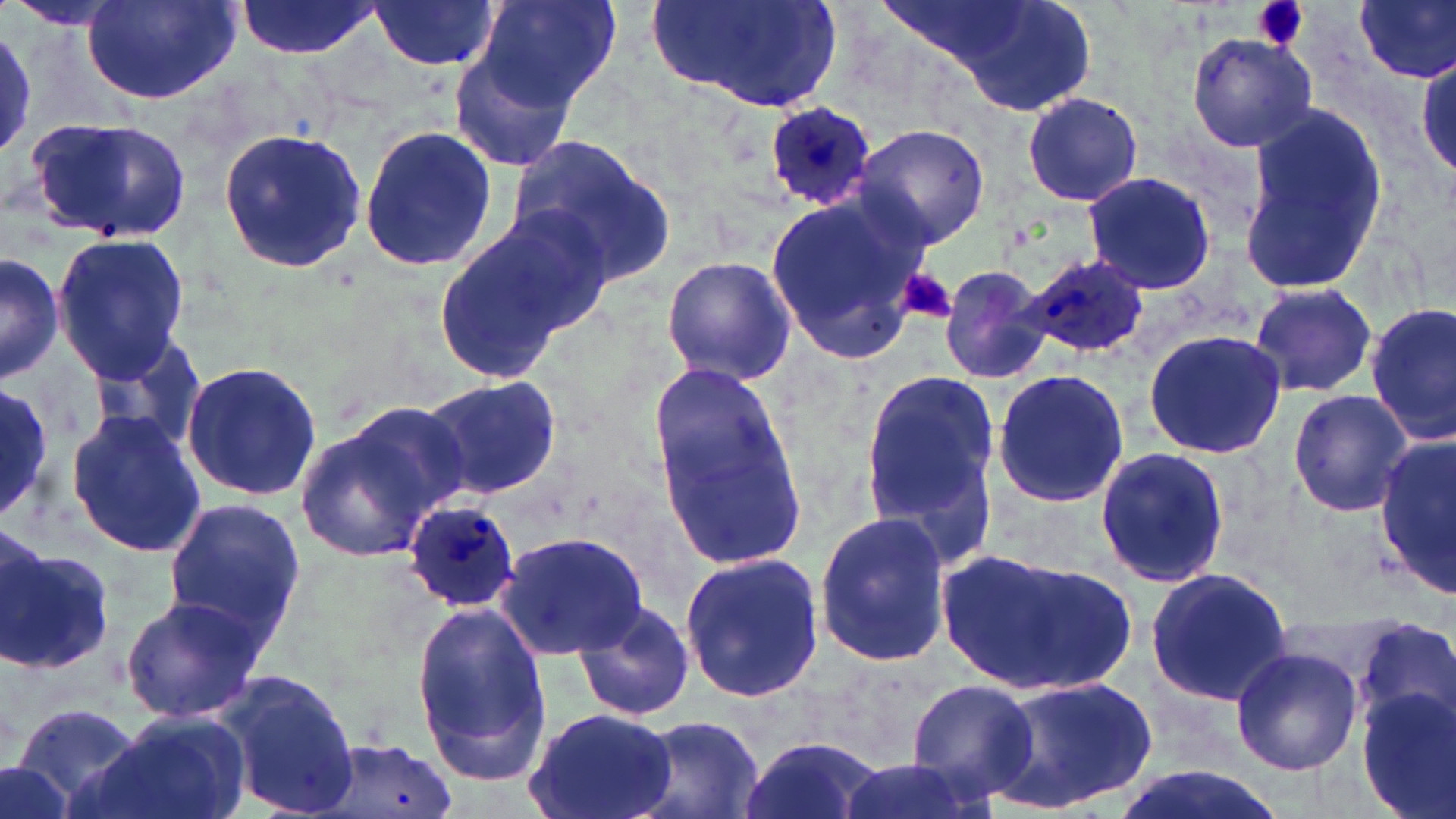
Summary:
  - Coordinate format: approximate bounding boxes as (x1,y1)-(x2,y2) corner pairs in pixels
  - Plasmodium ovale-infected red blood cell locations: (763,104)-(876,213), (1020,256)-(1151,362), (402,503)-(524,614)
  - Platelet locations: (1252,0)-(1309,53), (896,267)-(956,326)
  - Uninfected red blood cell locations: (237,0)-(379,58), (476,0)-(621,112), (650,0)-(844,115), (888,0)-(1103,115), (1355,0)-(1456,83), (82,1)-(240,104), (367,1)-(502,72), (4,2)-(129,31), (0,26)-(35,160), (1185,32)-(1319,154), (449,41)-(585,175), (1415,52)-(1456,184), (1021,91)-(1143,207), (1237,101)-(1393,299), (28,119)-(193,244), (357,123)-(500,276), (854,125)-(991,249), (217,128)-(368,274), (506,135)-(675,288), (1081,171)-(1217,293), (763,187)-(932,365), (432,209)-(605,382), (50,233)-(191,381), (1,252)-(62,383), (661,255)-(798,387), (937,264)-(1052,386), (1248,281)-(1380,397), (1367,302)-(1456,443), (1141,330)-(1286,461), (86,332)-(211,459), (180,359)-(325,502), (651,362)-(807,562), (857,366)-(1003,553), (990,370)-(1131,509), (419,375)-(561,503), (0,386)-(57,522), (1288,389)-(1414,516), (294,402)-(473,563), (65,411)-(207,558), (1375,433)-(1456,594), (1095,446)-(1232,589), (163,496)-(307,657), (813,512)-(954,666), (496,529)-(648,661), (0,538)-(113,679), (939,549)-(1136,694), (678,550)-(824,705), (1143,566)-(1294,709), (120,595)-(265,722), (573,599)-(699,721), (411,602)-(552,782), (1352,616)-(1456,733), (1228,645)-(1360,777), (211,669)-(362,816), (985,675)-(1158,812), (905,678)-(1040,799), (1355,687)-(1456,819), (12,701)-(147,814), (523,706)-(679,819), (84,712)-(248,819), (631,713)-(769,819), (735,735)-(886,819), (320,737)-(459,819), (828,751)-(987,819), (0,760)-(78,819), (1106,764)-(1289,819)
  - Slide-level diagnosis: Plasmodium ovale
  - Preparation: thin blood film
  - Magnification: 1000x
  - Image size: 1456×819 pixels
  - Field of view: one of a larger specimen
  - Modality: optical microscopy
  - Stain: May-Grünwald-Giemsa